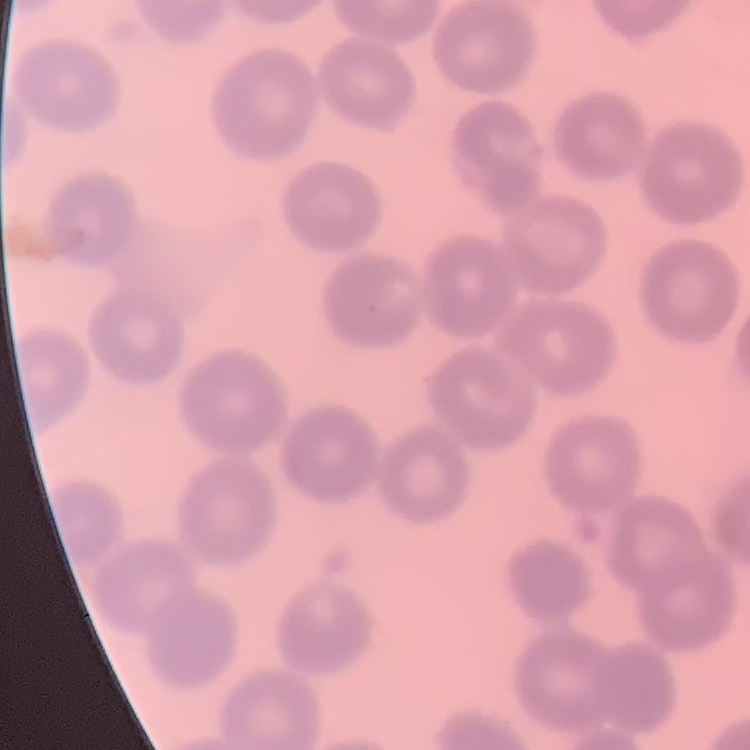

Summary:
  - Red blood cell morphology: no rouleaux formation
  - Stain: Field's or Giemsa
  - Image type: square crop of a larger photomicrograph
  - Preparation: thin peripheral smear